Outline each blood parasite and name the species.
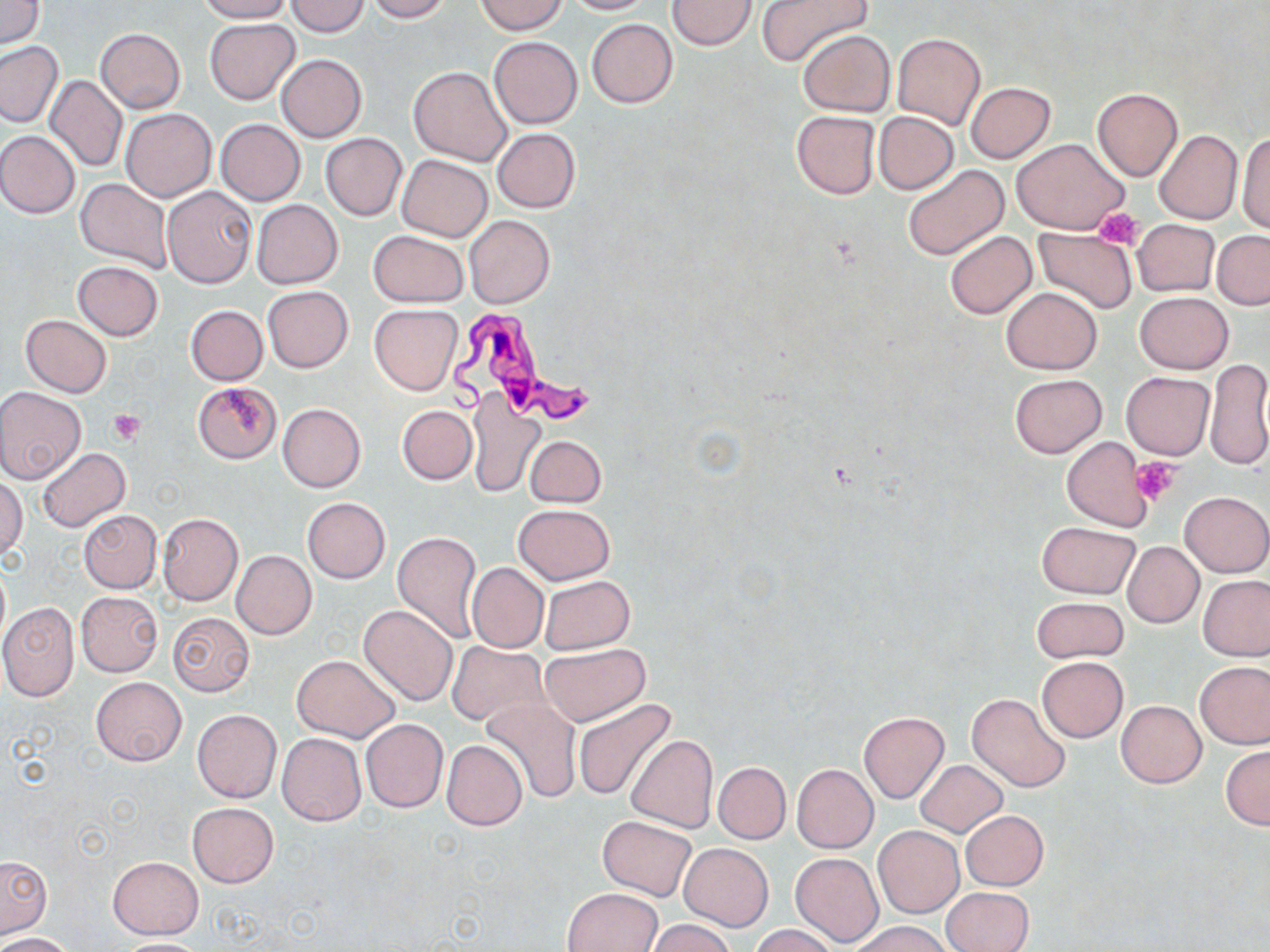
Approximate bounding boxes as named x1/y1/x2/y2 corners in pixels.
Trypanosoma brucei: (x1=442, y1=303, x2=604, y2=430).
No Plasmodium falciparum, Plasmodium ovale, Plasmodium malariae, Plasmodium vivax, or Babesia divergens observed.

slide-level diagnosis = Trypanosoma brucei
image size = 1270×952 pixels
stain = May-Grünwald-Giemsa
platelet locations = approximate bounding boxes as named x1/y1/x2/y2 corners in pixels: (x1=1094, y1=206, x2=1143, y2=248), (x1=108, y1=409, x2=147, y2=444), (x1=1132, y1=458, x2=1179, y2=503)
uninfected red blood cell locations = approximate bounding boxes as named x1/y1/x2/y2 corners in pixels: (x1=0, y1=0, x2=44, y2=48), (x1=195, y1=0, x2=295, y2=23), (x1=364, y1=0, x2=452, y2=22), (x1=562, y1=0, x2=656, y2=15), (x1=666, y1=0, x2=758, y2=51), (x1=758, y1=0, x2=872, y2=67), (x1=286, y1=1, x2=371, y2=36), (x1=477, y1=1, x2=568, y2=34), (x1=204, y1=18, x2=300, y2=104), (x1=586, y1=19, x2=677, y2=107), (x1=95, y1=27, x2=185, y2=113), (x1=798, y1=30, x2=894, y2=117), (x1=893, y1=33, x2=985, y2=129), (x1=488, y1=37, x2=583, y2=129), (x1=0, y1=39, x2=64, y2=128), (x1=277, y1=54, x2=367, y2=143), (x1=5, y1=56, x2=117, y2=158), (x1=409, y1=66, x2=511, y2=166), (x1=45, y1=76, x2=128, y2=171), (x1=965, y1=82, x2=1056, y2=162), (x1=1092, y1=87, x2=1184, y2=181), (x1=121, y1=109, x2=216, y2=201), (x1=791, y1=111, x2=879, y2=199), (x1=874, y1=112, x2=957, y2=193), (x1=215, y1=119, x2=305, y2=206), (x1=493, y1=128, x2=580, y2=213), (x1=1236, y1=129, x2=1270, y2=234), (x1=1154, y1=130, x2=1242, y2=225), (x1=0, y1=131, x2=81, y2=219), (x1=321, y1=133, x2=407, y2=220), (x1=1013, y1=138, x2=1129, y2=234), (x1=397, y1=154, x2=493, y2=241), (x1=904, y1=164, x2=1009, y2=260), (x1=75, y1=179, x2=173, y2=274), (x1=162, y1=185, x2=257, y2=289), (x1=252, y1=199, x2=343, y2=288), (x1=465, y1=215, x2=555, y2=308), (x1=1133, y1=218, x2=1219, y2=297), (x1=1034, y1=229, x2=1139, y2=314), (x1=369, y1=230, x2=466, y2=306), (x1=1212, y1=231, x2=1270, y2=310), (x1=945, y1=232, x2=1037, y2=318), (x1=71, y1=261, x2=162, y2=341), (x1=262, y1=286, x2=353, y2=373), (x1=1002, y1=287, x2=1102, y2=374), (x1=1134, y1=292, x2=1234, y2=374), (x1=369, y1=304, x2=463, y2=394), (x1=185, y1=305, x2=268, y2=384), (x1=21, y1=314, x2=112, y2=396), (x1=1204, y1=359, x2=1270, y2=471), (x1=1121, y1=372, x2=1214, y2=460), (x1=1010, y1=373, x2=1106, y2=457), (x1=194, y1=381, x2=281, y2=462), (x1=0, y1=387, x2=86, y2=484), (x1=466, y1=389, x2=546, y2=499), (x1=277, y1=403, x2=366, y2=493), (x1=398, y1=405, x2=477, y2=483), (x1=524, y1=435, x2=607, y2=507), (x1=1062, y1=436, x2=1154, y2=531), (x1=37, y1=448, x2=130, y2=532), (x1=1, y1=476, x2=26, y2=560), (x1=1180, y1=491, x2=1270, y2=577), (x1=302, y1=497, x2=390, y2=582), (x1=514, y1=503, x2=615, y2=584), (x1=79, y1=510, x2=162, y2=593), (x1=157, y1=513, x2=244, y2=605), (x1=1036, y1=521, x2=1140, y2=599), (x1=392, y1=530, x2=483, y2=644), (x1=1123, y1=542, x2=1204, y2=628), (x1=232, y1=550, x2=317, y2=639), (x1=467, y1=561, x2=548, y2=653), (x1=1199, y1=574, x2=1270, y2=661), (x1=540, y1=576, x2=635, y2=654), (x1=75, y1=591, x2=163, y2=676), (x1=1031, y1=597, x2=1128, y2=662), (x1=0, y1=603, x2=79, y2=701), (x1=359, y1=605, x2=458, y2=707), (x1=167, y1=611, x2=255, y2=696), (x1=446, y1=642, x2=549, y2=728), (x1=540, y1=643, x2=650, y2=726), (x1=292, y1=654, x2=398, y2=742), (x1=1037, y1=657, x2=1128, y2=742), (x1=1196, y1=660, x2=1270, y2=749), (x1=91, y1=677, x2=186, y2=767), (x1=968, y1=693, x2=1072, y2=792), (x1=481, y1=695, x2=583, y2=803), (x1=573, y1=699, x2=679, y2=800), (x1=1116, y1=700, x2=1206, y2=788), (x1=192, y1=709, x2=282, y2=803), (x1=859, y1=712, x2=949, y2=803), (x1=361, y1=718, x2=448, y2=812), (x1=277, y1=733, x2=366, y2=826), (x1=625, y1=734, x2=718, y2=833), (x1=442, y1=739, x2=527, y2=831), (x1=1221, y1=745, x2=1270, y2=830), (x1=915, y1=759, x2=1008, y2=838), (x1=713, y1=761, x2=791, y2=844), (x1=791, y1=764, x2=879, y2=853), (x1=187, y1=802, x2=279, y2=887), (x1=960, y1=810, x2=1049, y2=890), (x1=597, y1=816, x2=697, y2=899), (x1=873, y1=826, x2=964, y2=917), (x1=680, y1=843, x2=772, y2=931), (x1=789, y1=852, x2=883, y2=948), (x1=0, y1=856, x2=52, y2=938), (x1=108, y1=857, x2=203, y2=939), (x1=562, y1=887, x2=664, y2=952), (x1=943, y1=887, x2=1033, y2=952), (x1=646, y1=919, x2=737, y2=952), (x1=853, y1=920, x2=950, y2=952), (x1=750, y1=925, x2=841, y2=952), (x1=1, y1=932, x2=74, y2=952), (x1=110, y1=939, x2=213, y2=952)
modality = light microscopy
magnification = 1000x
preparation = thin blood film
field of view = one of a larger specimen